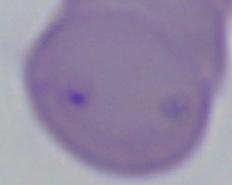
magnification: 1000x
modality: photomicrograph
identification: Babesia